Assess this cell for malaria.
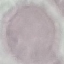
It is uninfected.

Giemsa-stained preparation. Photographed with a smartphone camera at the microscope eyepiece. Automatically extracted cell patch, resized to 64 × 64 pixels. Thin blood smear.